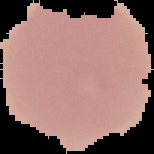

Summary:
  - Preparation: thin blood smear
  - Image size: 154×154 pixels
  - Result: negative for malaria parasites
  - Image type: cell region segmented out of the field of view; surrounding area masked to black